Report the malaria status of this cell.
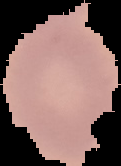
Uninfected.

Cell region segmented out of the field of view; the surrounding area is masked to black. Image is 121×166 pixels. From a thin blood smear.